Evaluate for parasitized red blood cells.
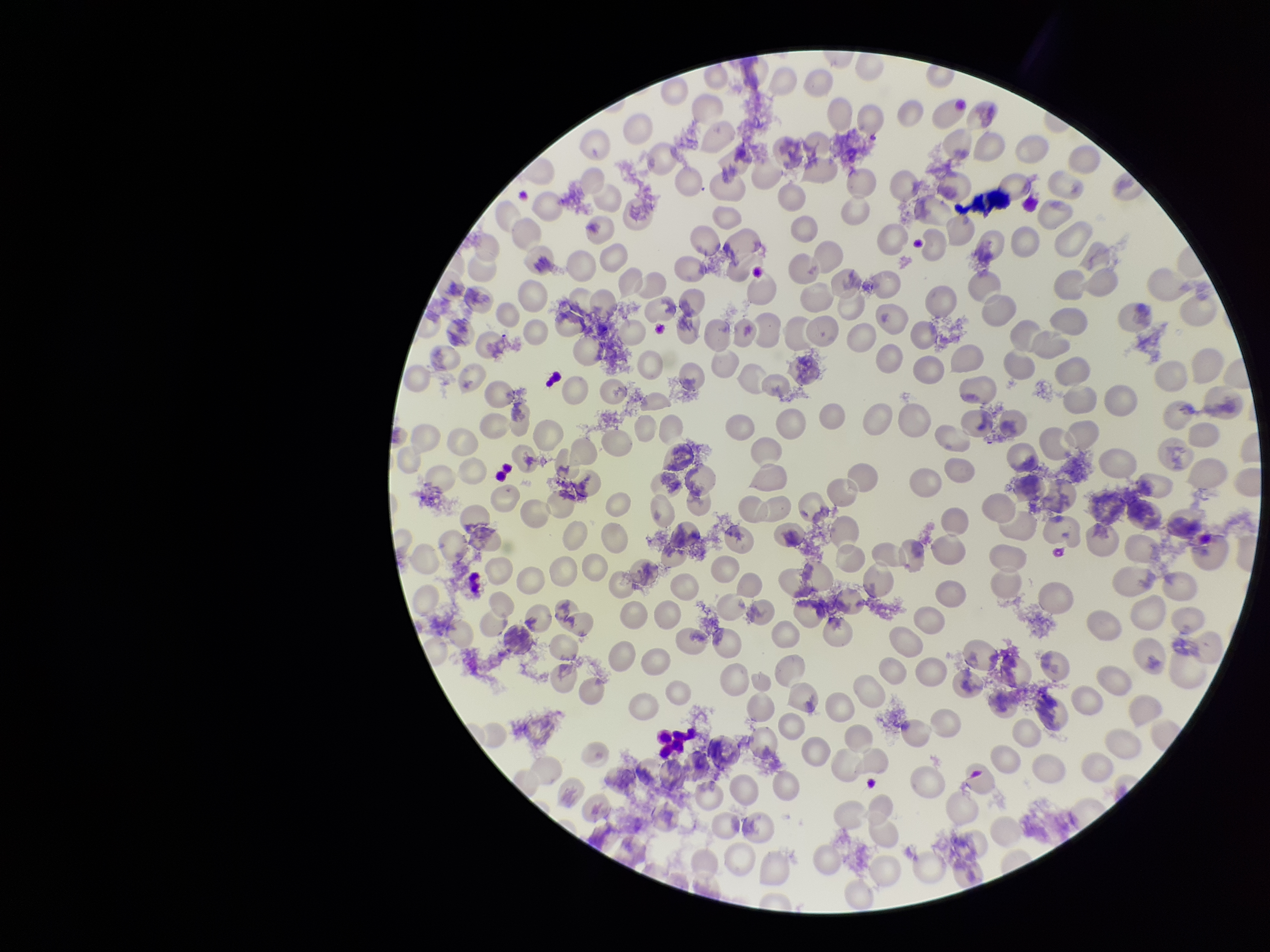
None identified.

preparation = thin blood smear
red blood cell count = 231
stain = Giemsa
image size = 1270×952 pixels
parasitized red blood cell count = 0
capture = smartphone photograph through the microscope eyepiece
patient malaria status = negative
field of view = single